Assess this cell for malaria.
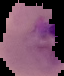
Parasitized.

From a thin blood film. Image is 64×76 pixels. The area outside the segmented cell region is set to black.